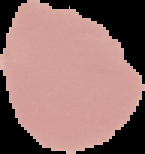
From a thin blood film. Malaria status: uninfected. Cell region segmented out of the field of view; the surrounding area is masked to black. Image is 145×154 pixels.